Locate every Plasmodium parasite and every leukocyte.
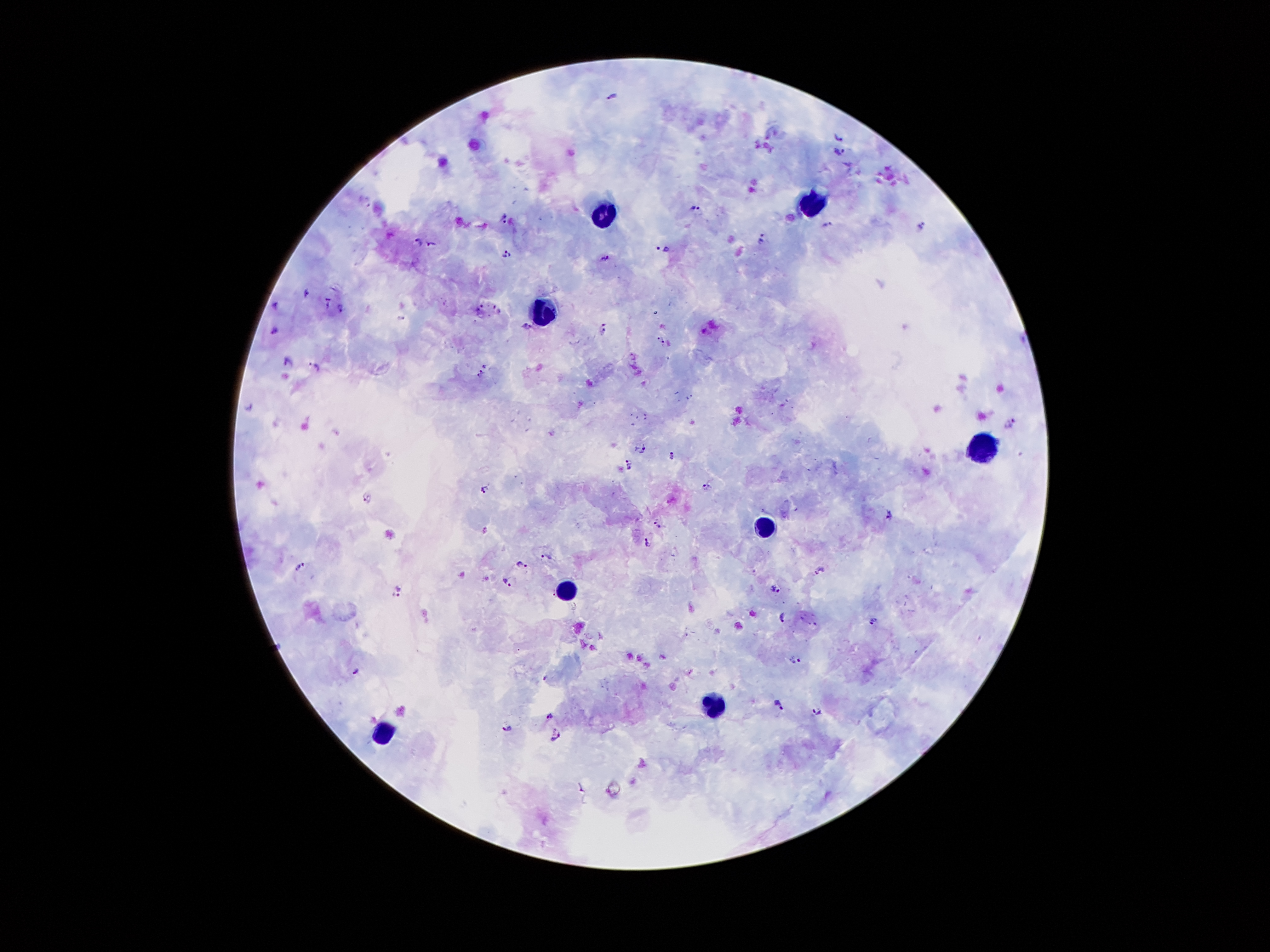
Approximate object centers, in pixels from the top-left corner.
Plasmodium parasites: (x=611, y=95), (x=838, y=138), (x=840, y=151), (x=695, y=209), (x=503, y=216), (x=827, y=224), (x=922, y=225), (x=763, y=239), (x=418, y=240), (x=432, y=243), (x=662, y=248), (x=506, y=253), (x=605, y=257), (x=306, y=292), (x=327, y=303), (x=275, y=305), (x=478, y=307), (x=341, y=308), (x=497, y=309), (x=528, y=327), (x=274, y=332), (x=604, y=332), (x=661, y=340), (x=290, y=363), (x=314, y=366), (x=481, y=373), (x=249, y=406), (x=1009, y=422), (x=644, y=450), (x=671, y=455), (x=629, y=465), (x=705, y=489), (x=484, y=491), (x=367, y=497), (x=888, y=514), (x=657, y=524), (x=647, y=542), (x=547, y=558), (x=522, y=563), (x=300, y=567), (x=818, y=570), (x=509, y=582), (x=775, y=590), (x=398, y=592), (x=781, y=617), (x=874, y=619), (x=796, y=659), (x=356, y=671), (x=545, y=678), (x=779, y=705), (x=818, y=711), (x=550, y=717), (x=507, y=727), (x=556, y=737).
Leukocytes: (x=816, y=198), (x=601, y=209), (x=545, y=304), (x=983, y=447), (x=759, y=530), (x=561, y=592), (x=715, y=702), (x=382, y=737).

Summary:
  - Preparation: thick peripheral-blood smear
  - Patient malaria status: positive for Plasmodium falciparum
  - Stain: Giemsa
  - Capture: smartphone through the microscope eyepiece
  - Magnification: 100x
  - Image size: 1270×952 pixels
  - Field of view: single